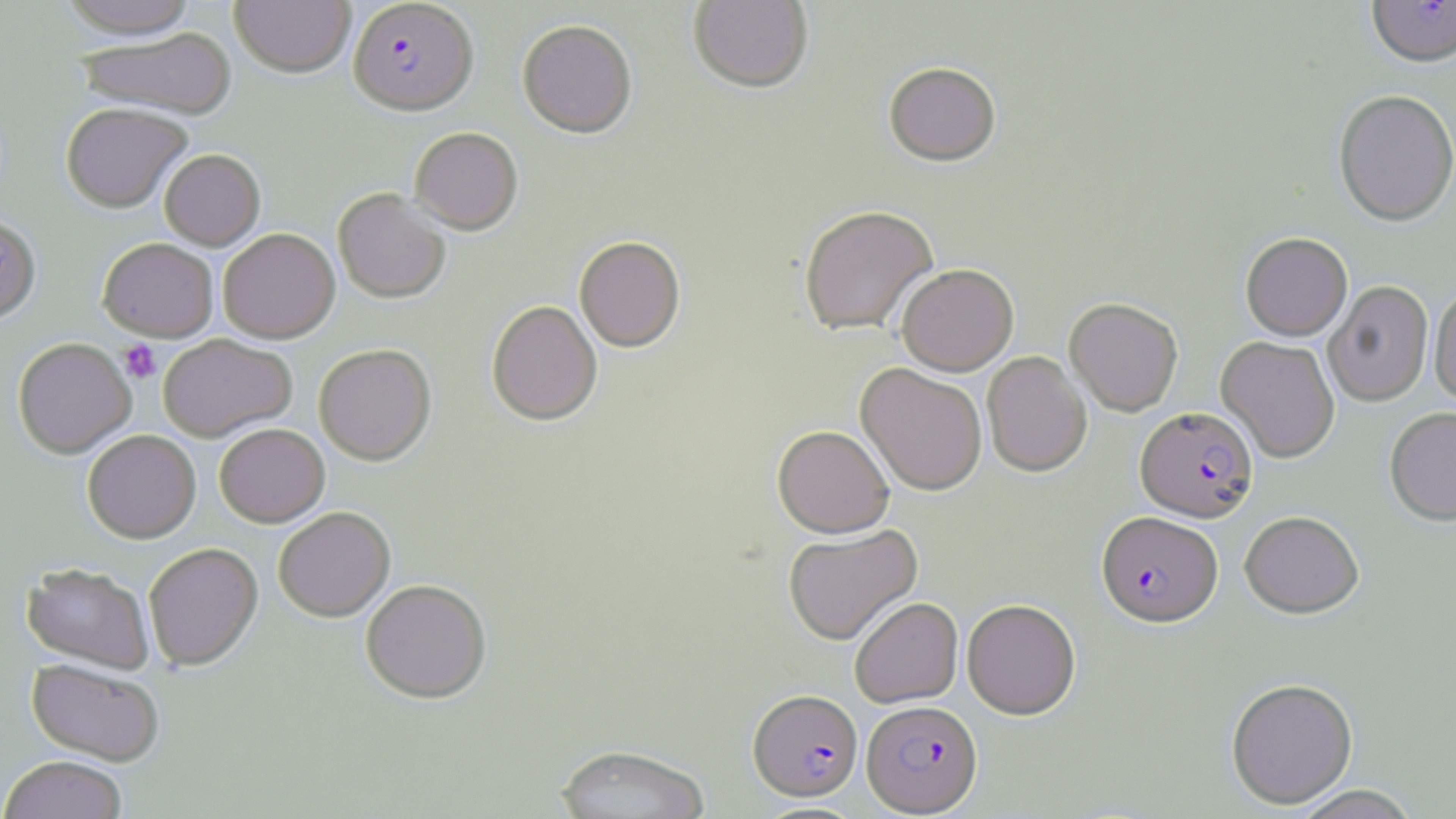
Summary:
  - Coordinate format: approximate bounding boxes as named x1/y1/x2/y2 corners in pixels
  - Uninfected red blood cell locations: (x1=56, y1=0, x2=201, y2=39), (x1=230, y1=0, x2=355, y2=77), (x1=689, y1=0, x2=813, y2=95), (x1=518, y1=20, x2=637, y2=138), (x1=76, y1=28, x2=237, y2=120), (x1=883, y1=64, x2=1001, y2=169), (x1=1333, y1=91, x2=1455, y2=228), (x1=61, y1=102, x2=192, y2=213), (x1=410, y1=127, x2=523, y2=234), (x1=159, y1=149, x2=265, y2=250), (x1=333, y1=188, x2=451, y2=303), (x1=798, y1=205, x2=940, y2=338), (x1=0, y1=214, x2=41, y2=323), (x1=218, y1=228, x2=340, y2=343), (x1=1241, y1=233, x2=1352, y2=341), (x1=97, y1=237, x2=219, y2=341), (x1=574, y1=237, x2=685, y2=353), (x1=897, y1=265, x2=1019, y2=377), (x1=1324, y1=281, x2=1433, y2=407), (x1=1430, y1=283, x2=1456, y2=408), (x1=1064, y1=298, x2=1184, y2=417), (x1=486, y1=300, x2=603, y2=426), (x1=158, y1=333, x2=297, y2=441), (x1=1216, y1=336, x2=1340, y2=463), (x1=13, y1=337, x2=136, y2=458), (x1=313, y1=344, x2=436, y2=464), (x1=982, y1=352, x2=1092, y2=477), (x1=855, y1=363, x2=988, y2=497), (x1=1384, y1=408, x2=1456, y2=527), (x1=214, y1=423, x2=329, y2=527), (x1=772, y1=426, x2=894, y2=539), (x1=82, y1=429, x2=201, y2=543), (x1=273, y1=506, x2=395, y2=621), (x1=1239, y1=511, x2=1365, y2=619), (x1=784, y1=524, x2=923, y2=646), (x1=143, y1=542, x2=263, y2=670), (x1=22, y1=563, x2=154, y2=673), (x1=360, y1=578, x2=492, y2=703), (x1=850, y1=597, x2=963, y2=708), (x1=962, y1=599, x2=1081, y2=720), (x1=26, y1=659, x2=164, y2=766), (x1=1226, y1=678, x2=1358, y2=810), (x1=554, y1=743, x2=712, y2=819), (x1=0, y1=755, x2=128, y2=819), (x1=1291, y1=786, x2=1424, y2=819)
  - Plasmodium falciparum-infected red blood cell locations: (x1=348, y1=1, x2=479, y2=115), (x1=1366, y1=1, x2=1456, y2=70), (x1=1135, y1=408, x2=1258, y2=523), (x1=1096, y1=512, x2=1223, y2=629), (x1=749, y1=690, x2=863, y2=802), (x1=862, y1=700, x2=983, y2=816)
  - Platelet locations: (x1=119, y1=340, x2=161, y2=383)
  - Slide-level diagnosis: Plasmodium falciparum
  - Magnification: 1000x
  - Field of view: single
  - Stain: May-Grünwald-Giemsa
  - Modality: optical microscopy
  - Preparation: thin blood smear
  - Image size: 1456×819 pixels